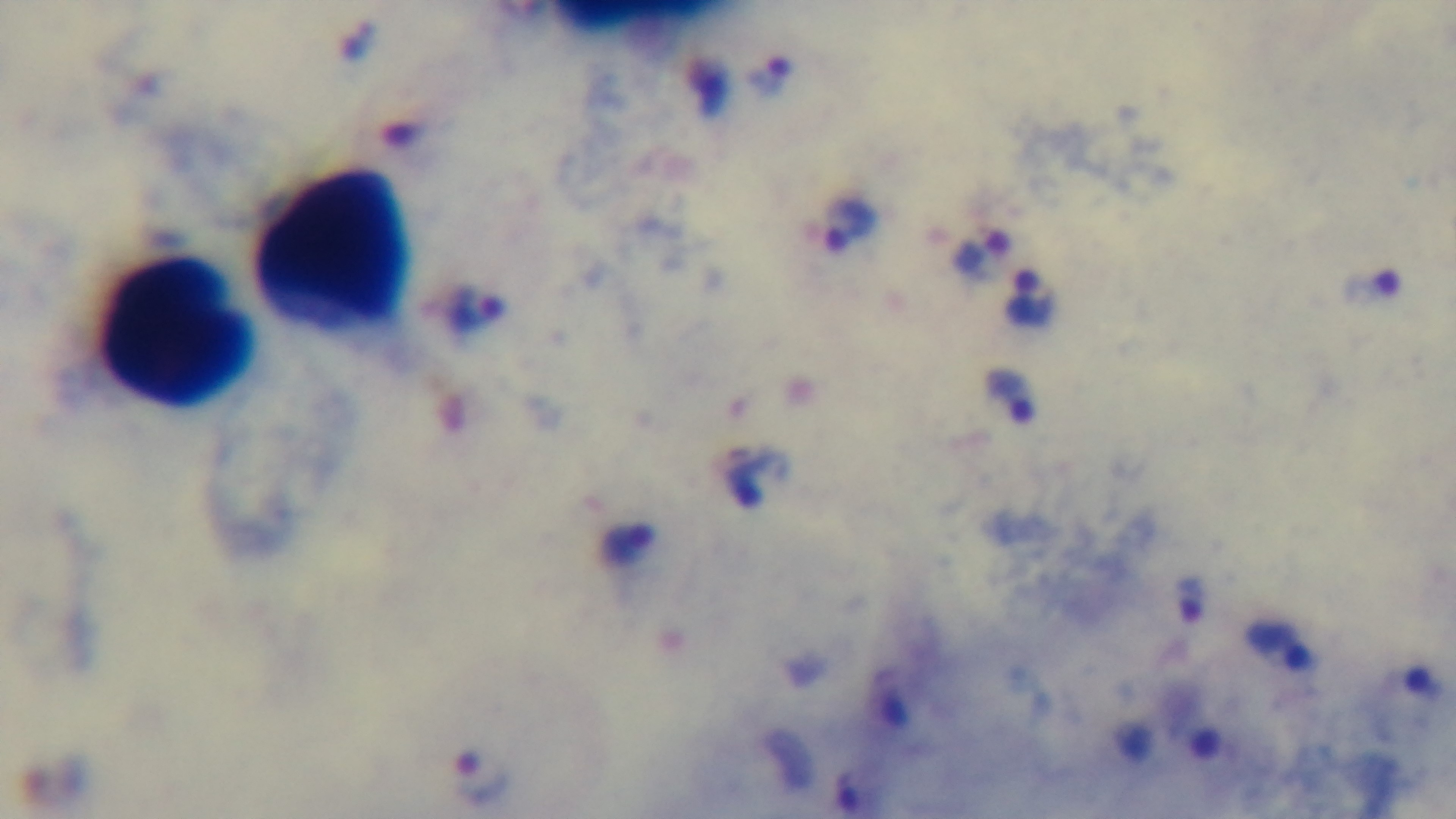

capture = mounted 4K digital camera
field of view = one from the slide
stain = Giemsa
modality = light microscopy
preparation = thick
objective = 100x oil immersion
malaria status = infected